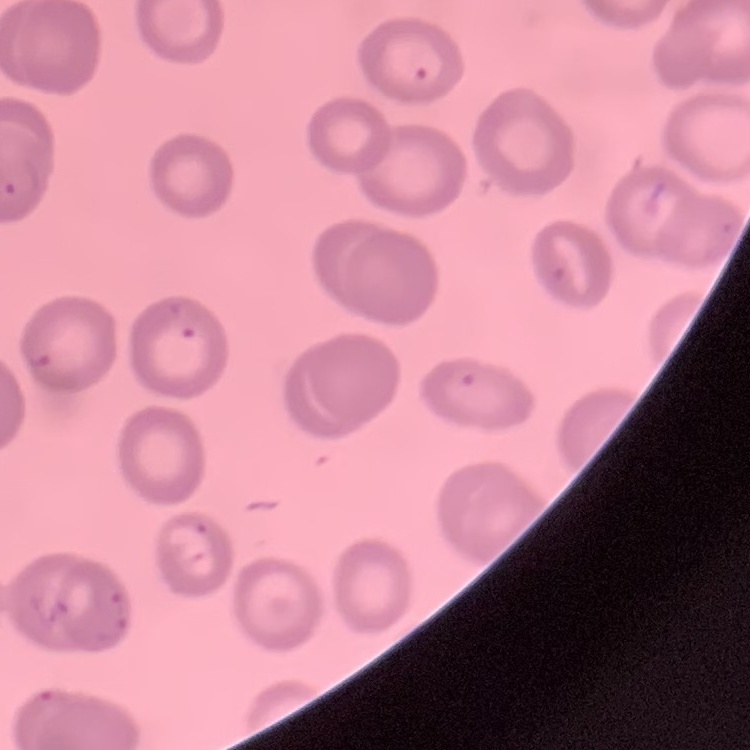

Summary:
  - Erythrocyte morphology: no rouleaux formation
  - Preparation: thin peripheral smear
  - Stain: Field's or Giemsa
  - Image type: square crop of a larger photomicrograph